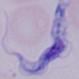
A trypanosome is shown. Captured at 1000x magnification. Photomicrograph.